Report the malaria status of this cell.
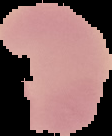
Uninfected.

image type = segmented cell region with the area outside set to black
preparation = thin blood smear
image size = 112×136 pixels